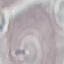

Result: no malaria parasites seen. Giemsa stain. Photographed with a smartphone camera at the microscope eyepiece. Cell patch, automatically extracted from a larger field of view and resized to 64 × 64 pixels. Thin blood smear.